Classify this cell by malaria status.
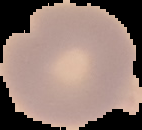
Uninfected.

image_type: segmented cell region on a black background
image_size: 142×130 pixels
preparation: thin blood smear